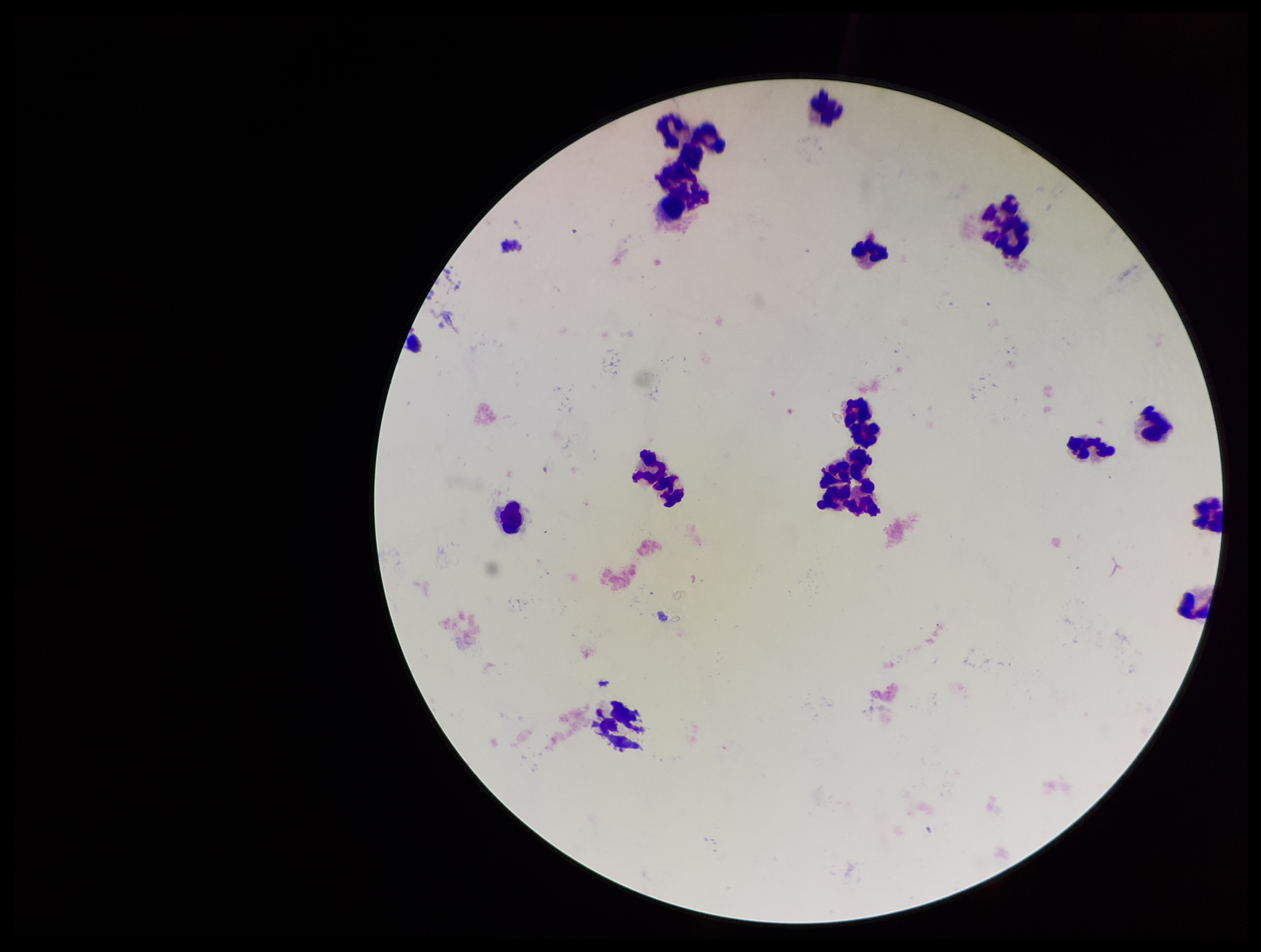

Plasmodium parasites: none detected. Patient malaria status: negative. Giemsa stain. Photographed through the microscope eyepiece with a smartphone camera. Preparation: thick blood smear. One field from this slide. Leukocyte count: 18. Parasite count: 0. Image is 1261×952 pixels.